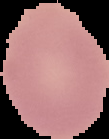

Summary:
  - Result: no Plasmodium parasites detected
  - Image type: segmented cell region with the area outside set to black
  - Preparation: thin blood smear
  - Image size: 109×139 pixels